Assess this cell for malaria.
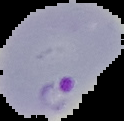
Parasitized.

From a thin blood film. Image is 124×121 pixels. Segmented cell region on a black background.